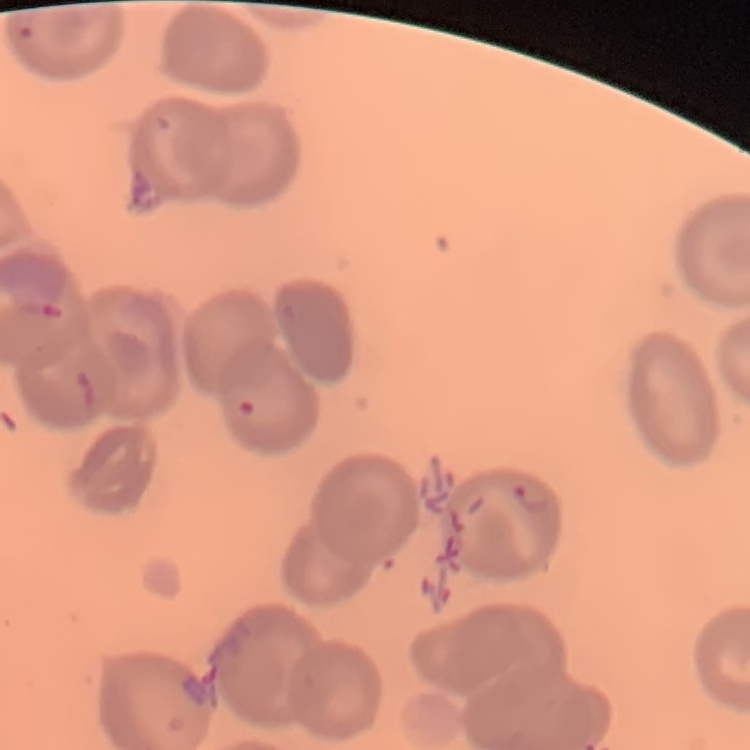 The red blood cells show no rouleaux formation. Stained with either Field's or Giemsa. One tile cut from a larger photomicrograph. Thin peripheral smear.